Name the cell type shown.
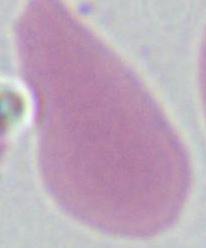

An erythrocyte.

Micrograph. 1000x magnification.